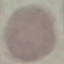
Summary:
  - Result: no malaria parasites detected
  - Image type: cell patch, automatically extracted from a larger field of view and resized to 64 × 64 pixels
  - Preparation: thin blood smear
  - Capture: smartphone through the microscope eyepiece
  - Stain: Giemsa